Comment on the morphology of the red blood cells.
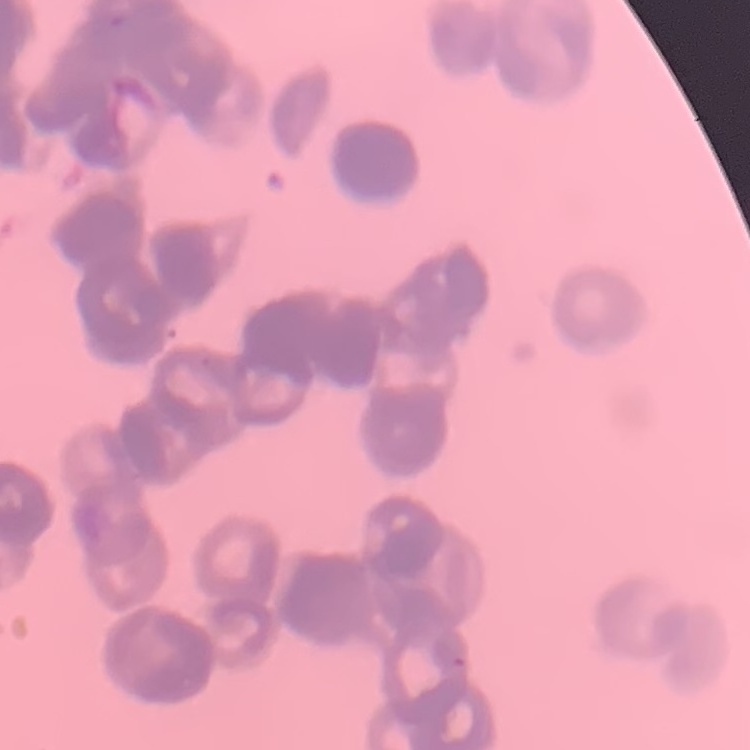

Rouleaux formation.

Thin blood smear. Square crop of a larger photomicrograph. Stained with either Field's or Giemsa.